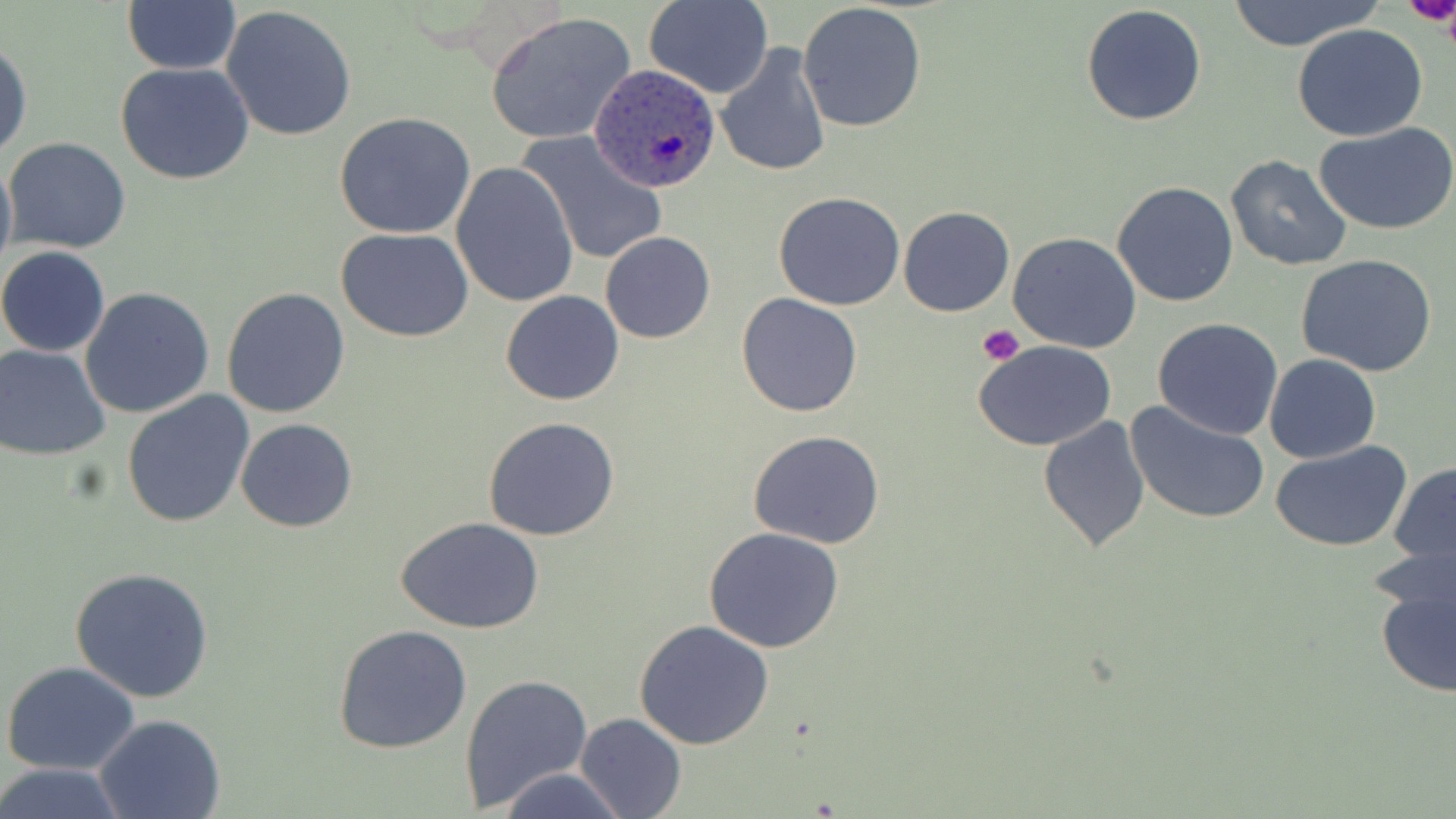
slide-level diagnosis = Plasmodium ovale
magnification = 1000x
preparation = thin blood smear
platelet locations = approximate bounding boxes as named x1/y1/x2/y2 corners in pixels: (x1=1400, y1=0, x2=1454, y2=32), (x1=977, y1=325, x2=1024, y2=365)
image size = 1456×819 pixels
Plasmodium ovale-infected red blood cell locations = approximate bounding boxes as named x1/y1/x2/y2 corners in pixels: (x1=590, y1=62, x2=723, y2=193)
uninfected red blood cell locations = approximate bounding boxes as named x1/y1/x2/y2 corners in pixels: (x1=646, y1=0, x2=772, y2=98), (x1=1219, y1=0, x2=1384, y2=52), (x1=1400, y1=0, x2=1456, y2=30), (x1=121, y1=1, x2=241, y2=73), (x1=798, y1=3, x2=928, y2=133), (x1=1081, y1=4, x2=1208, y2=127), (x1=221, y1=6, x2=360, y2=142), (x1=485, y1=12, x2=637, y2=145), (x1=1293, y1=24, x2=1428, y2=142), (x1=0, y1=36, x2=32, y2=161), (x1=714, y1=41, x2=832, y2=179), (x1=116, y1=61, x2=257, y2=185), (x1=334, y1=113, x2=477, y2=240), (x1=1315, y1=121, x2=1456, y2=235), (x1=514, y1=128, x2=669, y2=266), (x1=4, y1=137, x2=132, y2=255), (x1=0, y1=148, x2=16, y2=286), (x1=1225, y1=156, x2=1353, y2=271), (x1=450, y1=161, x2=580, y2=308), (x1=1112, y1=180, x2=1239, y2=306), (x1=774, y1=191, x2=907, y2=311), (x1=898, y1=205, x2=1015, y2=317), (x1=335, y1=228, x2=476, y2=344), (x1=601, y1=231, x2=716, y2=344), (x1=1010, y1=233, x2=1142, y2=354), (x1=0, y1=245, x2=110, y2=356), (x1=1296, y1=253, x2=1439, y2=377), (x1=222, y1=286, x2=351, y2=417), (x1=79, y1=287, x2=216, y2=418), (x1=501, y1=290, x2=624, y2=405), (x1=736, y1=294, x2=862, y2=418), (x1=1153, y1=317, x2=1285, y2=440), (x1=974, y1=339, x2=1118, y2=453), (x1=1, y1=345, x2=113, y2=460), (x1=1264, y1=354, x2=1380, y2=463), (x1=121, y1=390, x2=256, y2=528), (x1=1125, y1=400, x2=1271, y2=526), (x1=482, y1=415, x2=623, y2=541), (x1=1039, y1=415, x2=1151, y2=554), (x1=236, y1=417, x2=358, y2=532), (x1=747, y1=429, x2=885, y2=550), (x1=1269, y1=441, x2=1414, y2=551), (x1=1388, y1=462, x2=1456, y2=572), (x1=395, y1=517, x2=545, y2=634), (x1=703, y1=526, x2=847, y2=653), (x1=1372, y1=553, x2=1456, y2=700), (x1=71, y1=566, x2=214, y2=704), (x1=635, y1=621, x2=775, y2=751), (x1=332, y1=625, x2=474, y2=756), (x1=2, y1=661, x2=141, y2=775), (x1=460, y1=673, x2=592, y2=815), (x1=575, y1=712, x2=686, y2=817), (x1=95, y1=715, x2=224, y2=819), (x1=0, y1=763, x2=128, y2=818), (x1=494, y1=767, x2=630, y2=819)
stain = May-Grünwald-Giemsa
field of view = single
modality = optical microscopy